Identify the parasite.
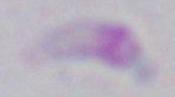

This is Toxoplasma gondii.

modality = micrograph
magnification = 1000x